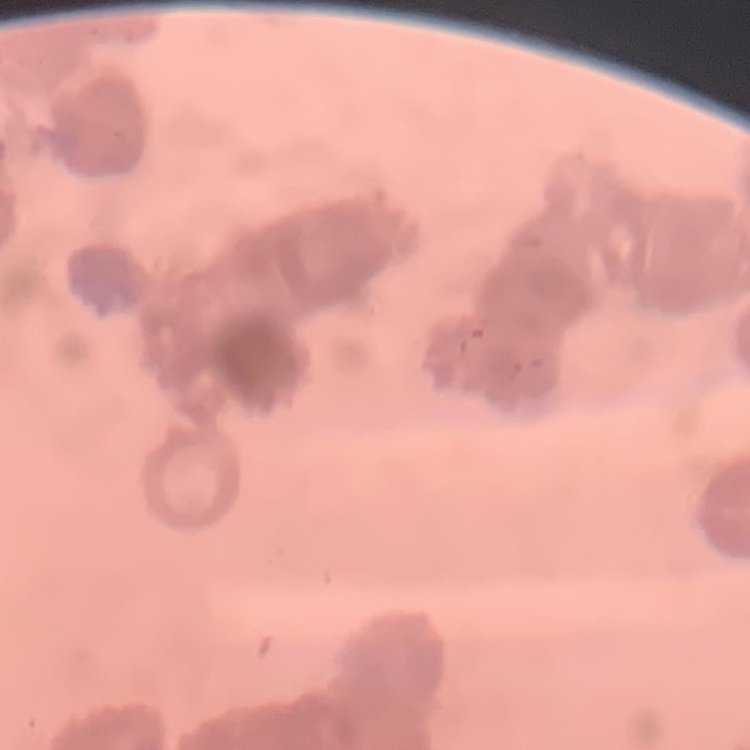
red blood cell morphology = rouleaux formation
image type = one tile cut from a larger photomicrograph
stain = Field's or Giemsa
preparation = thin peripheral smear